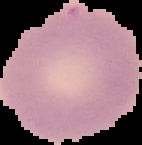
{
  "malaria_status": "uninfected",
  "image_size": "142×145 pixels",
  "image_type": "segmented cell region on a black background",
  "preparation": "thin blood film"
}